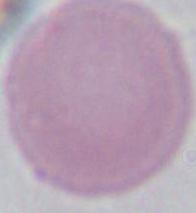

Summary:
  - Identification: erythrocyte
  - Modality: micrograph
  - Magnification: 1000x